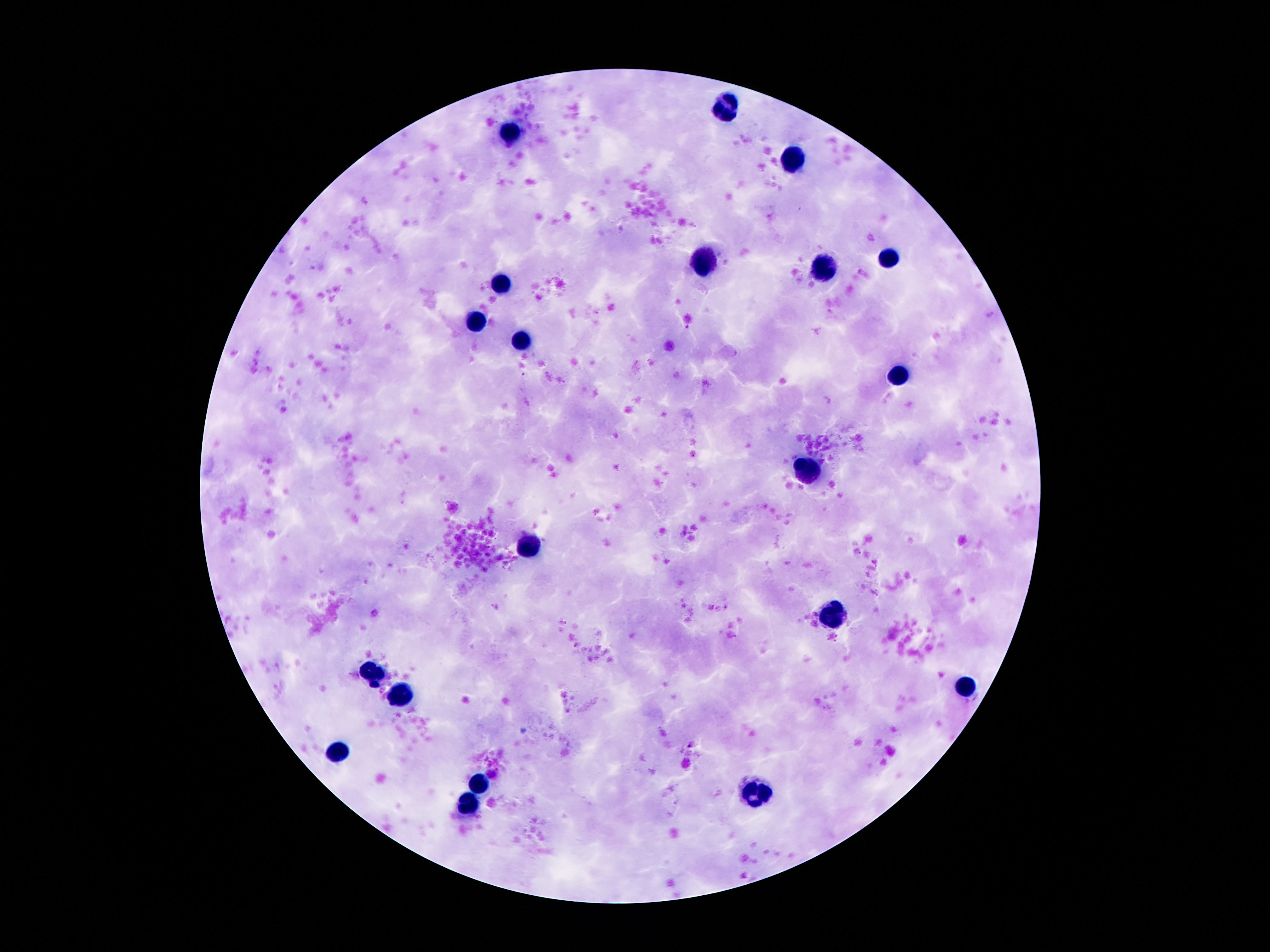 Approximate centers as (x, y) in pixels. Leukocyte locations: (732, 106), (508, 135), (797, 159), (892, 256), (700, 263), (825, 266), (504, 282), (476, 322), (523, 342), (900, 376), (810, 470), (526, 543), (831, 613), (375, 675), (961, 688), (401, 695), (340, 751), (482, 781), (760, 792), (470, 808). Single field of view. Giemsa-stained preparation. 100x magnification. Photographed through the microscope eyepiece with a smartphone camera. Patient malaria status: not infected. Thick blood smear. Image is 1270×952 pixels.